Identify the cell.
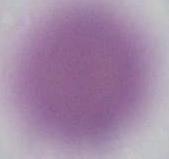

This is an erythrocyte.

Micrograph. 1000x magnification.